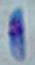
Summary:
  - Magnification: 1000x
  - Modality: micrograph
  - Identification: Toxoplasma gondii